Classify this cell by malaria status.
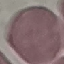
It is uninfected.

Automatically extracted cell patch, resized to 64 × 64 pixels. Giemsa stain. Acquired by smartphone through the microscope eyepiece. Thin smear of blood.